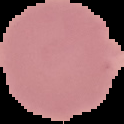

image type = segmented cell region with the area outside set to black
preparation = thin blood smear
result = negative for Plasmodium parasites
image size = 124×124 pixels